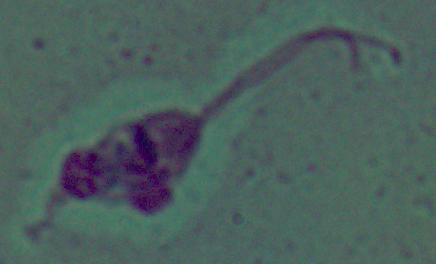
Summary:
  - Magnification: 1000x
  - Identification: Leishmania
  - Modality: micrograph